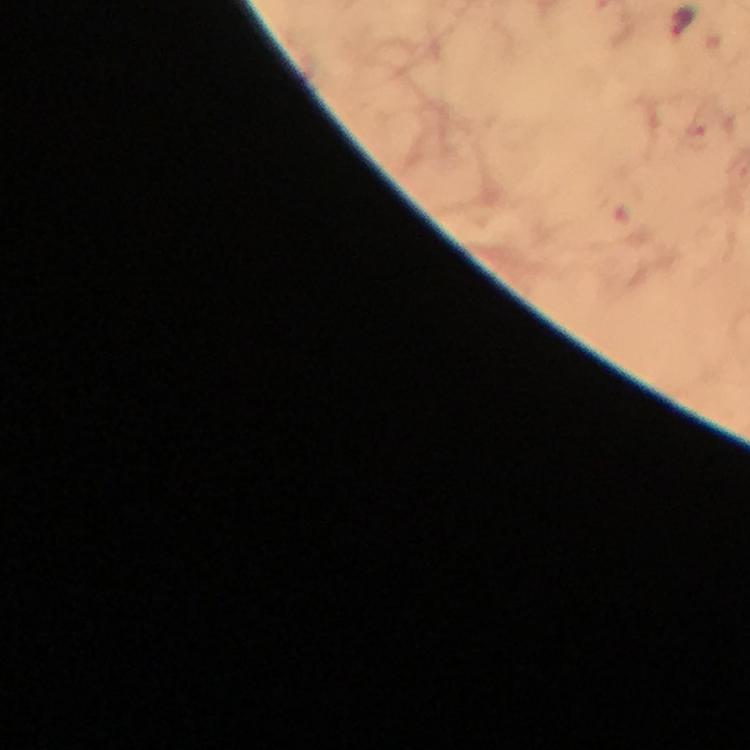
Approximate centers as {x, y} in pixels.
Summary:
  - Malaria parasite locations: {682, 22}
  - Context: from a diagnostic examination for malaria
  - Capture: smartphone mounted on the microscope
  - Preparation: thick blood smear
  - Magnification: 100x
  - Immersion oil: applied
  - Stain: Giemsa
  - Image size: 750×750 pixels
  - Cropped from: one field of view